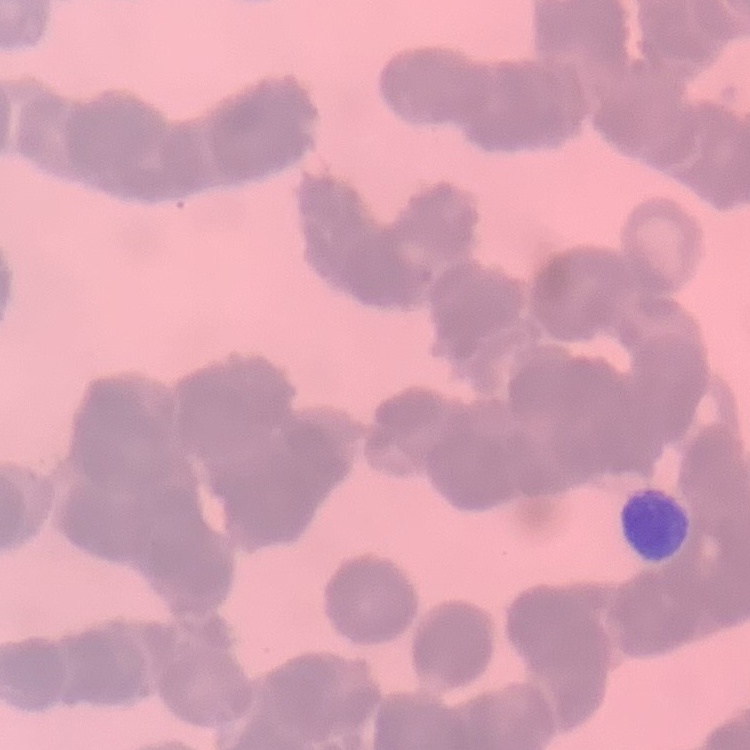

Summary:
  - Erythrocyte morphology: rouleaux formation
  - Preparation: thin blood film
  - Image type: one tile cut from a larger photomicrograph
  - Stain: Field's or Giemsa